Classify this cell by malaria status.
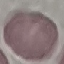
Uninfected.

image type = cell patch, automatically extracted from a larger field of view and resized to 64 × 64 pixels
stain = Giemsa
capture = smartphone camera at the microscope eyepiece
preparation = thin smear